Assess this cell for malaria.
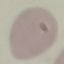
It is uninfected.

Thin blood film. Cell patch, automatically extracted from a larger field of view and resized to 64 × 64 pixels. Photographed with a smartphone camera at the microscope eyepiece. Giemsa stain.